Locate and identify every blood parasite.
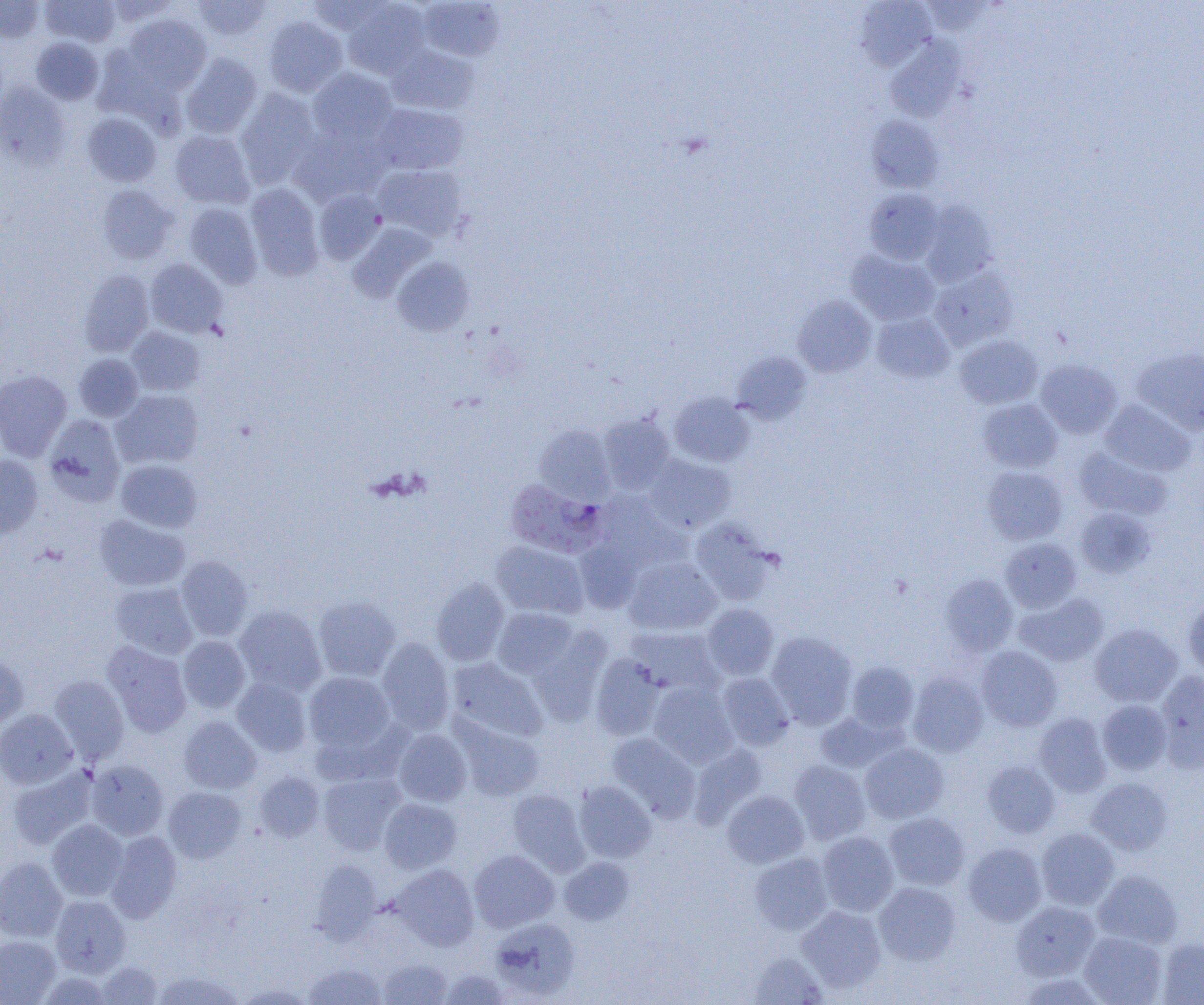
Approximate bounding boxes as [x1, y1, x2, y2] in pixels.
Plasmodium falciparum-infected red blood cells: [505, 479, 605, 558].
No Plasmodium ovale, Plasmodium malariae, Plasmodium vivax, Babesia divergens, or Trypanosoma brucei observed.

slide-level diagnosis = Plasmodium falciparum
uninfected red blood cell locations = approximate bounding boxes as [x1, y1, x2, y2] in pixels: [0, 0, 44, 42], [41, 0, 121, 47], [104, 0, 178, 27], [193, 0, 271, 41], [305, 0, 390, 36], [343, 1, 431, 78], [418, 1, 505, 61], [855, 1, 937, 71], [124, 13, 212, 93], [264, 15, 348, 97], [31, 37, 104, 104], [886, 37, 966, 122], [387, 45, 478, 115], [181, 53, 262, 138], [307, 67, 398, 145], [0, 82, 71, 169], [235, 89, 321, 188], [372, 103, 468, 176], [82, 112, 161, 186], [867, 115, 943, 192], [289, 125, 388, 208], [170, 130, 254, 209], [374, 164, 466, 241], [245, 183, 324, 280], [97, 184, 178, 264], [865, 188, 944, 265], [313, 189, 386, 265], [919, 200, 998, 287], [184, 202, 262, 287], [348, 224, 435, 302], [846, 251, 940, 326], [392, 256, 474, 336], [145, 258, 228, 338], [929, 266, 1019, 350], [79, 269, 154, 357], [792, 295, 877, 377], [872, 312, 954, 383], [126, 326, 205, 396], [954, 335, 1043, 409], [1132, 347, 1204, 434], [731, 351, 811, 424], [74, 353, 143, 421], [1036, 359, 1122, 439], [0, 370, 72, 461], [112, 389, 204, 468], [669, 392, 755, 467], [978, 398, 1062, 473], [1100, 400, 1195, 476], [598, 413, 674, 493], [44, 414, 126, 505], [534, 424, 616, 504], [1073, 446, 1172, 521], [0, 454, 43, 538], [645, 454, 736, 533], [115, 459, 202, 532], [982, 466, 1067, 545], [597, 494, 689, 569], [1075, 507, 1155, 578], [93, 515, 190, 591], [690, 519, 777, 605], [1001, 538, 1081, 612], [574, 539, 644, 613], [490, 541, 589, 619], [176, 556, 253, 641], [624, 557, 721, 635], [939, 574, 1018, 656], [431, 578, 509, 666], [110, 582, 197, 658], [1014, 593, 1108, 666], [314, 596, 401, 681], [1183, 598, 1204, 680], [702, 603, 779, 680], [234, 605, 326, 695], [492, 607, 577, 678], [1090, 623, 1183, 707], [528, 626, 613, 724], [626, 626, 724, 697], [766, 631, 857, 728], [178, 636, 250, 713], [377, 638, 455, 734], [102, 641, 192, 737], [976, 646, 1061, 731], [0, 653, 28, 729], [590, 653, 665, 740], [446, 658, 547, 743], [846, 661, 919, 734], [1155, 671, 1204, 771], [304, 672, 395, 754], [907, 672, 988, 757], [716, 673, 795, 750], [49, 675, 129, 763], [232, 677, 311, 756], [648, 682, 738, 767], [1097, 699, 1172, 774], [0, 709, 77, 788], [816, 711, 898, 773], [1034, 712, 1112, 797], [178, 716, 262, 794], [454, 718, 545, 802], [393, 728, 471, 807], [607, 733, 700, 822], [859, 742, 949, 823], [688, 744, 768, 829], [86, 760, 168, 840], [789, 760, 871, 844], [981, 760, 1060, 837], [7, 767, 98, 850], [255, 772, 324, 841], [318, 772, 406, 854], [1087, 777, 1173, 855], [573, 781, 656, 863], [163, 786, 246, 863], [507, 789, 590, 875], [722, 790, 809, 868], [379, 798, 462, 873], [884, 812, 970, 890], [47, 819, 127, 901], [1037, 827, 1119, 910], [105, 831, 181, 923], [817, 831, 898, 916], [963, 843, 1046, 926], [469, 849, 559, 932], [750, 852, 833, 934], [0, 857, 68, 941], [559, 857, 634, 924], [310, 860, 382, 942], [390, 864, 479, 950], [1092, 869, 1182, 948], [874, 882, 960, 965], [51, 895, 130, 976], [1011, 901, 1100, 980], [797, 905, 886, 992], [490, 917, 579, 1001], [1079, 930, 1167, 1005], [0, 936, 61, 1004], [1156, 937, 1204, 1004], [748, 952, 829, 1004], [378, 957, 452, 1004], [96, 962, 161, 1004], [303, 962, 386, 1005], [439, 969, 510, 1004], [151, 970, 244, 1005], [235, 982, 316, 1004]
magnification = 1000x
field of view = single
modality = optical microscopy
preparation = thin blood film
image size = 1204×1005 pixels